Identify the preparation type.
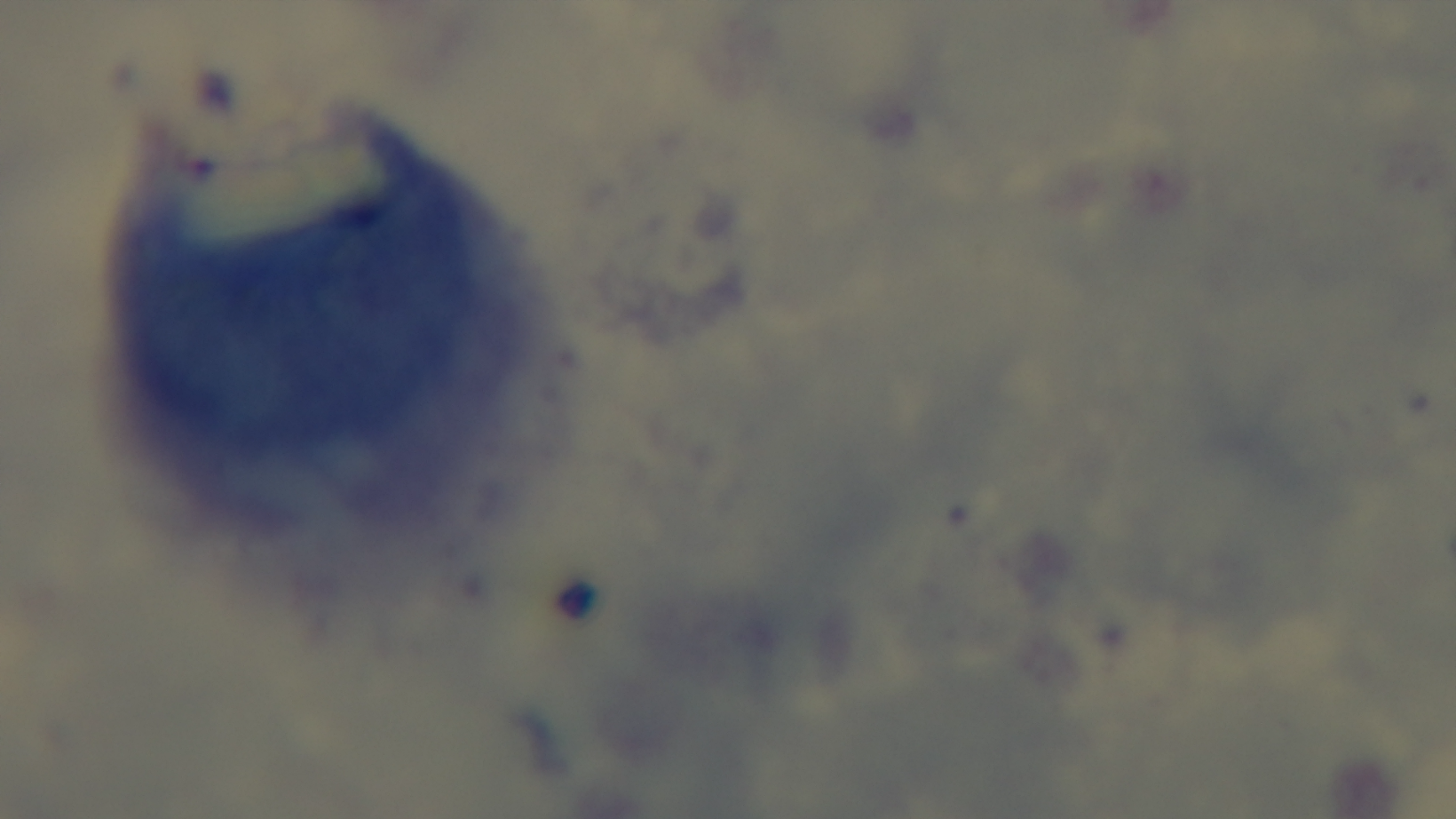

Thick.

{
  "objective": "100x oil immersion",
  "stain": "Giemsa",
  "modality": "light microscopy",
  "field_of_view": "one from the slide",
  "malaria_status": "uninfected",
  "capture": "mounted 4K digital camera"
}